Assess this cell for malaria.
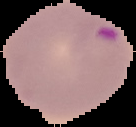

It is parasitized.

Image is 136×127 pixels. Segmented cell region on a black background. From a thin blood smear.